Describe the morphology of the erythrocytes.
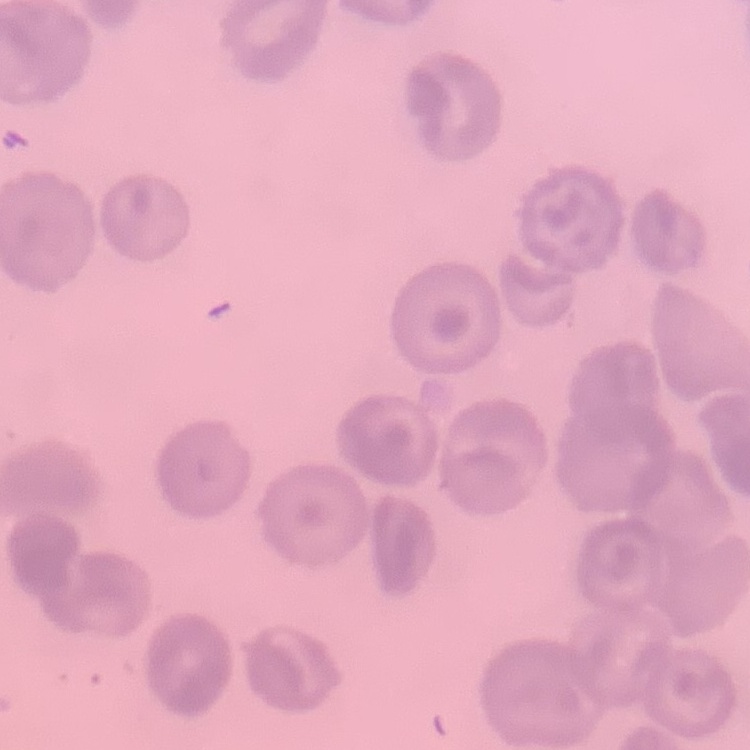
No rouleaux formation.

image type = one tile cut from a larger photomicrograph
stain = Field's or Giemsa
preparation = thin blood film